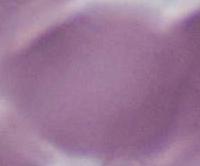 Photomicrograph. Captured at 1000x magnification. A red blood cell is shown.